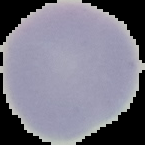 Image is 145×145 pixels. Malaria status: uninfected. From a thin blood film. The area outside the segmented cell region is set to black.